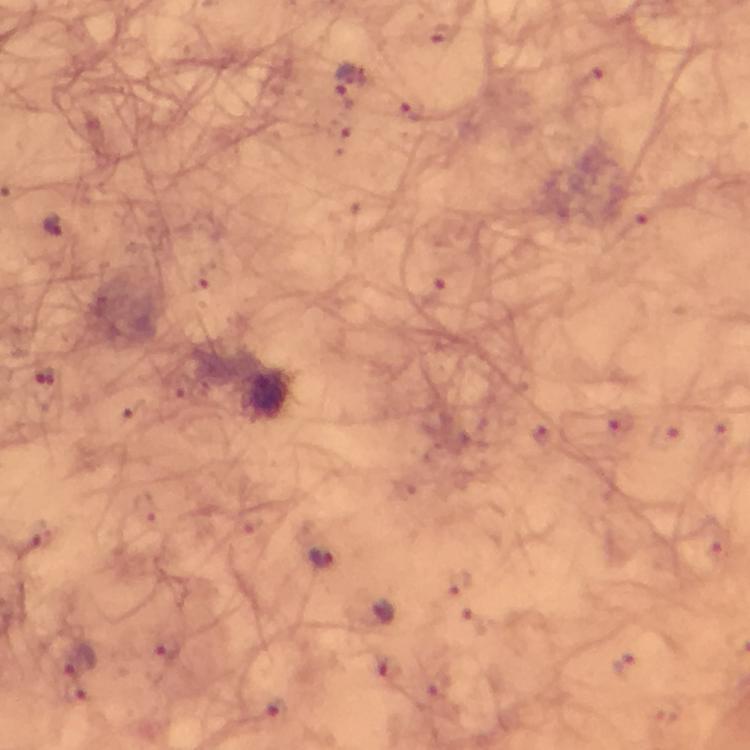
Approximate centers as [x, y] in pixels.
Summary:
  - Malaria parasite locations: [438, 32], [347, 80], [411, 110], [53, 225], [46, 384], [321, 558], [167, 647], [80, 662], [623, 665], [277, 710]
  - Magnification: 100x
  - Preparation: thick blood smear
  - Capture: smartphone mounted on the microscope
  - Image size: 750×750 pixels
  - Stain: Giemsa
  - Immersion oil: applied
  - Cropped from: one field of view
  - Context: from a diagnostic examination for malaria